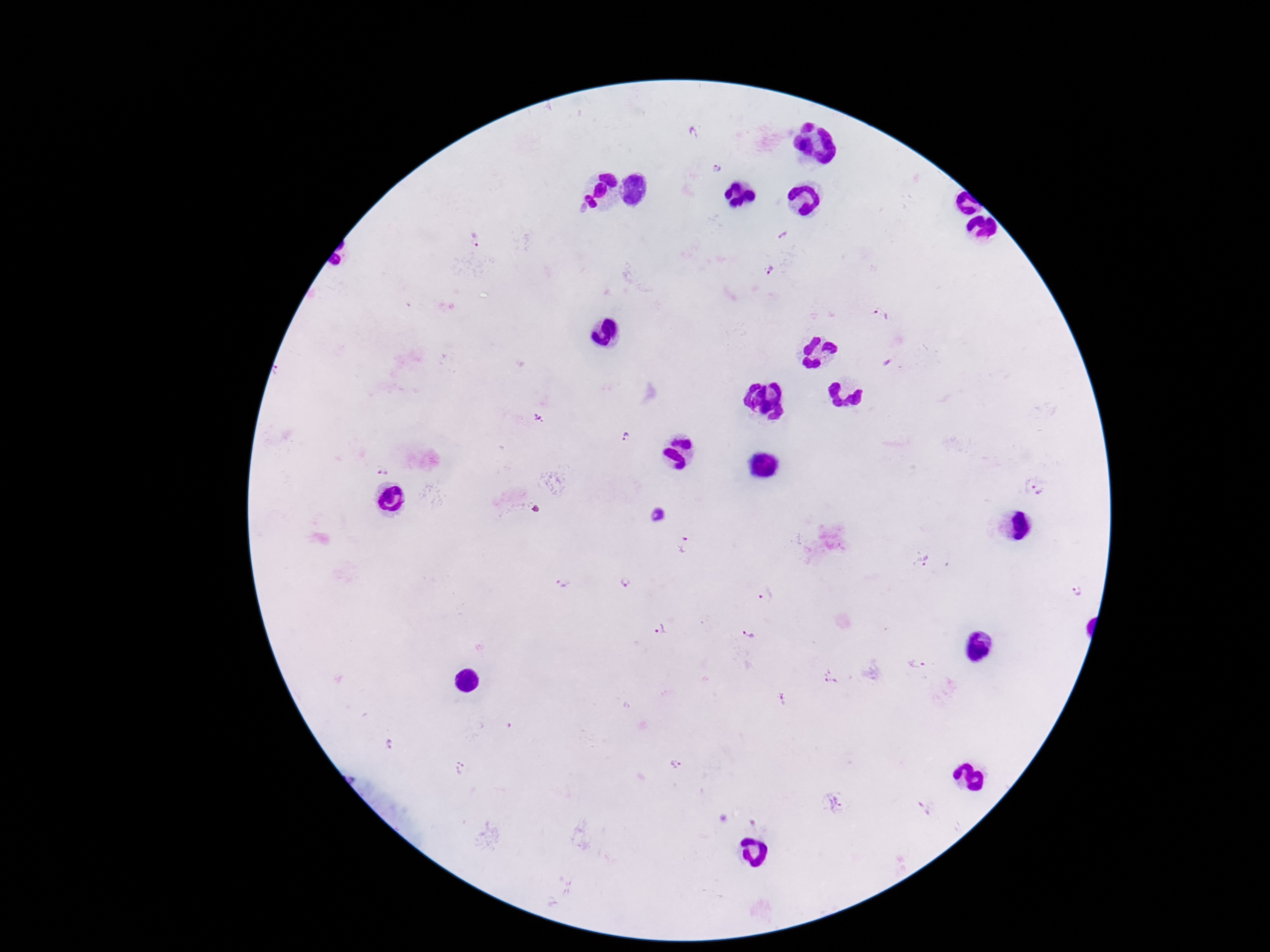
Approximate centers as [x, y] in pixels.
Summary:
  - Plasmodium parasite locations: [714, 167], [782, 235], [772, 268], [882, 311], [538, 420], [626, 437], [1037, 484], [658, 515], [687, 546], [921, 558], [631, 582], [567, 585], [1077, 591], [766, 597], [661, 629], [750, 634], [920, 663], [831, 679], [785, 697], [391, 745], [679, 767], [461, 769], [835, 802], [925, 807]
  - Magnification: 100x
  - Image size: 1270×952 pixels
  - Stain: Giemsa
  - Preparation: thick blood film
  - Field of view: one from this slide
  - Capture: smartphone camera through the microscope eyepiece
  - Patient malaria status: positive